Give the extent of all uninfected red blood cells.
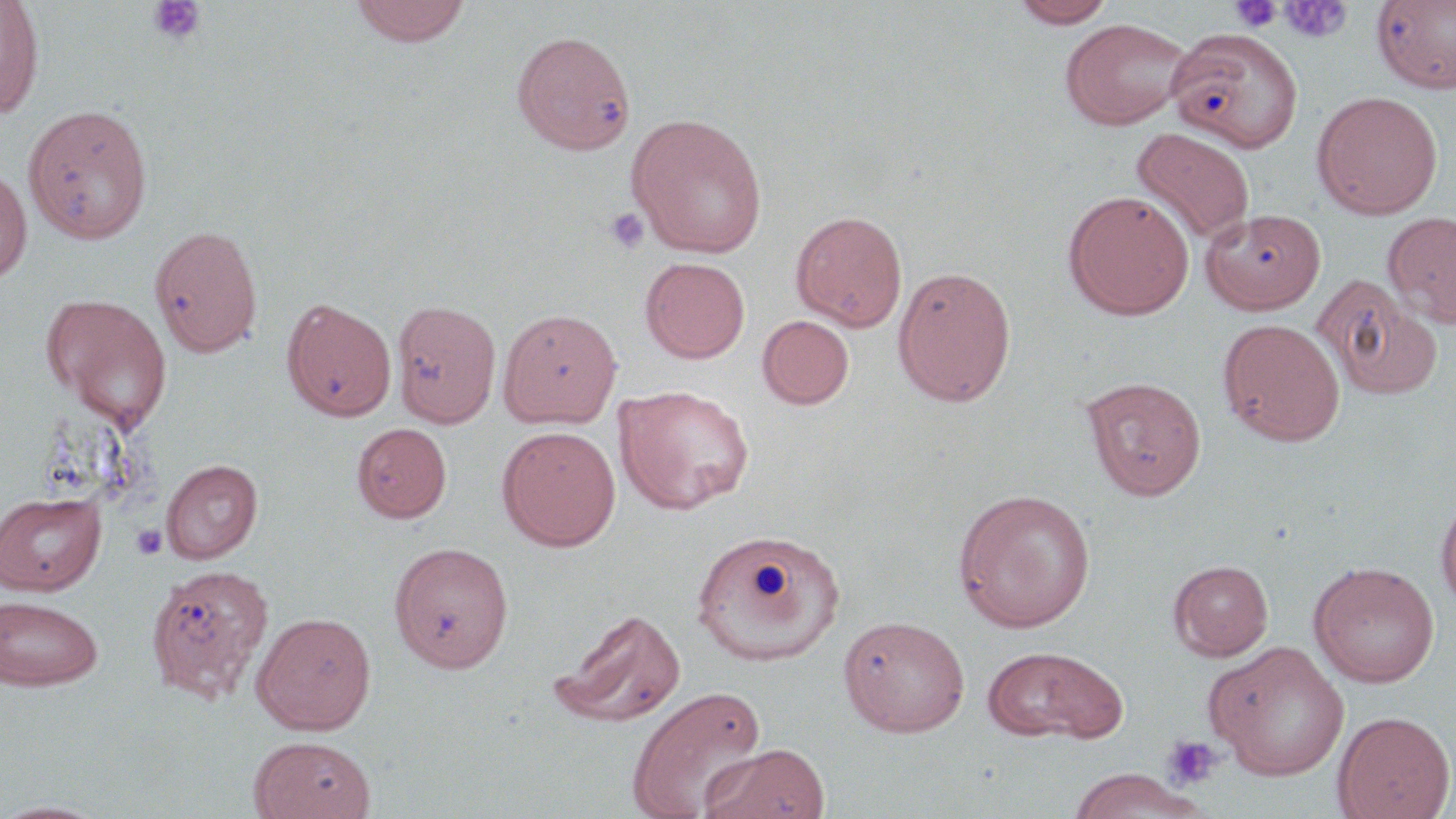
Approximate bounding boxes as (x1, y1, x2, y2) in pixels.
Uninfected red blood cells: (0, 0, 45, 120), (349, 0, 473, 47), (1010, 0, 1118, 28), (1371, 0, 1456, 93), (1060, 18, 1193, 130), (1166, 26, 1304, 153), (511, 30, 636, 155), (1312, 90, 1443, 219), (23, 103, 153, 244), (626, 113, 768, 258), (1130, 127, 1255, 247), (0, 167, 32, 285), (1062, 189, 1195, 320), (1201, 207, 1326, 314), (790, 210, 908, 331), (1383, 212, 1456, 329), (149, 224, 264, 358), (640, 257, 750, 363), (893, 265, 1017, 407), (1312, 274, 1443, 401), (42, 293, 172, 427), (281, 296, 397, 422), (390, 298, 502, 429), (498, 307, 621, 428), (757, 314, 855, 410), (1217, 318, 1346, 446), (1080, 374, 1207, 500), (614, 384, 755, 514), (351, 422, 452, 523), (497, 426, 621, 550), (160, 458, 263, 563), (951, 487, 1097, 632), (1435, 490, 1456, 610), (0, 491, 106, 595), (0, 496, 122, 678), (690, 528, 847, 666), (389, 541, 513, 673), (1169, 560, 1273, 660), (1308, 560, 1440, 688), (145, 562, 271, 703), (1, 595, 104, 690), (550, 608, 687, 729), (251, 610, 377, 735), (839, 615, 970, 737), (1205, 641, 1350, 781), (981, 645, 1127, 744), (626, 685, 767, 819), (1332, 710, 1455, 819), (248, 736, 376, 819), (701, 742, 831, 819), (1065, 768, 1207, 819), (0, 798, 113, 819).

slide-level diagnosis = negative for blood parasites
field of view = single
preparation = thin blood smear
stain = May-Grünwald-Giemsa
magnification = 1000x
image size = 1456×819 pixels
platelet locations = approximate bounding boxes as (x1, y1, x2, y2) in pixels: (148, 1, 206, 45), (1229, 1, 1283, 33), (1280, 2, 1352, 44), (604, 207, 650, 255), (131, 524, 167, 560), (1163, 734, 1223, 790)
modality = optical microscopy